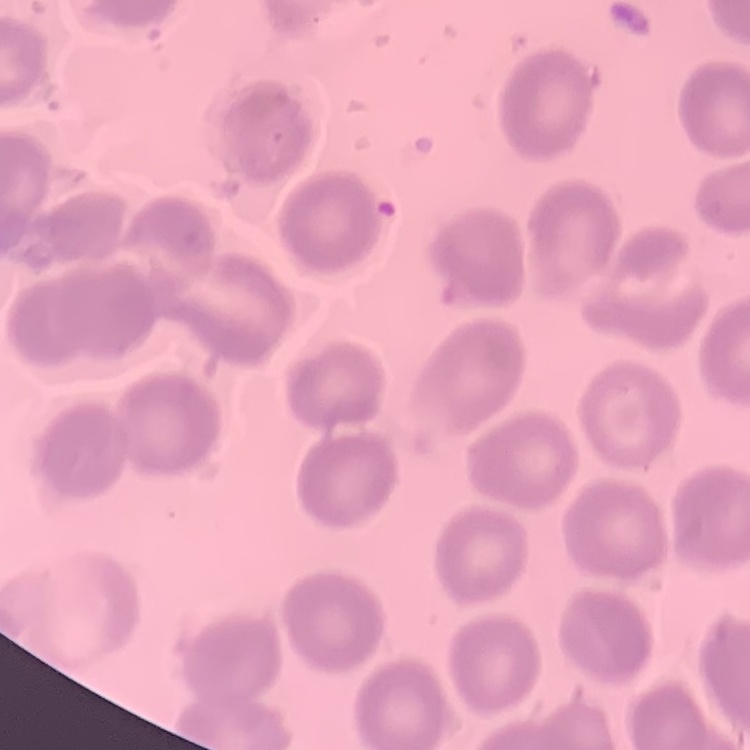
The red blood cells show no rouleaux formation. Stained with either Field's or Giemsa. One tile cut from a larger photomicrograph. Thin blood smear.